State which cell type is depicted.
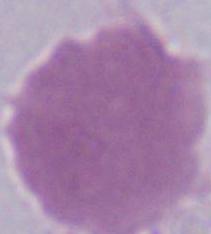

This is an erythrocyte.

Captured at 1000x magnification. Micrograph.